Comment on the morphology of the red blood cells.
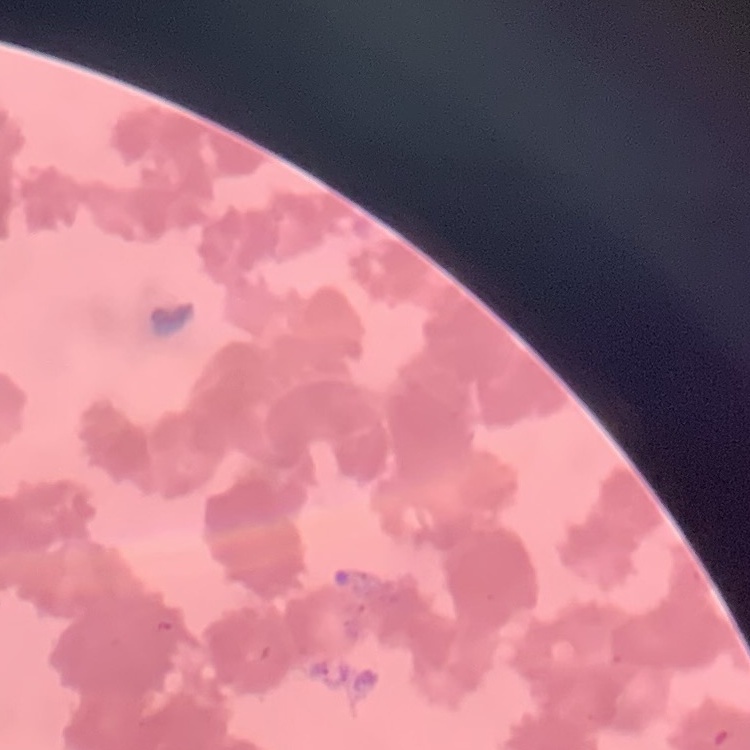

They show rouleaux formation.

Summary:
  - Stain: Field's or Giemsa
  - Image type: one tile cut from a larger photomicrograph
  - Preparation: thin peripheral smear